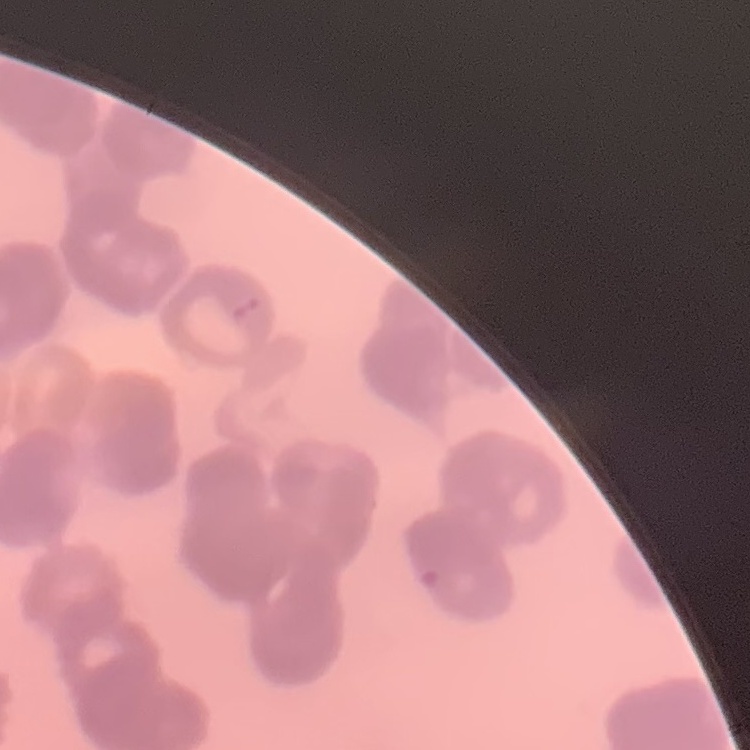
Summary:
  - Erythrocyte morphology: rouleaux formation
  - Image type: one tile cut from a larger photomicrograph
  - Stain: Field's or Giemsa
  - Preparation: thin blood smear